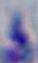
Summary:
  - Modality: photomicrograph
  - Identification: Toxoplasma gondii
  - Magnification: 1000x